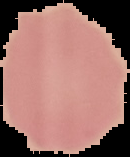
image_size: 130×157 pixels
malaria_status: uninfected
image_type: cell region segmented out of the field of view; surrounding area masked to black
preparation: thin blood film